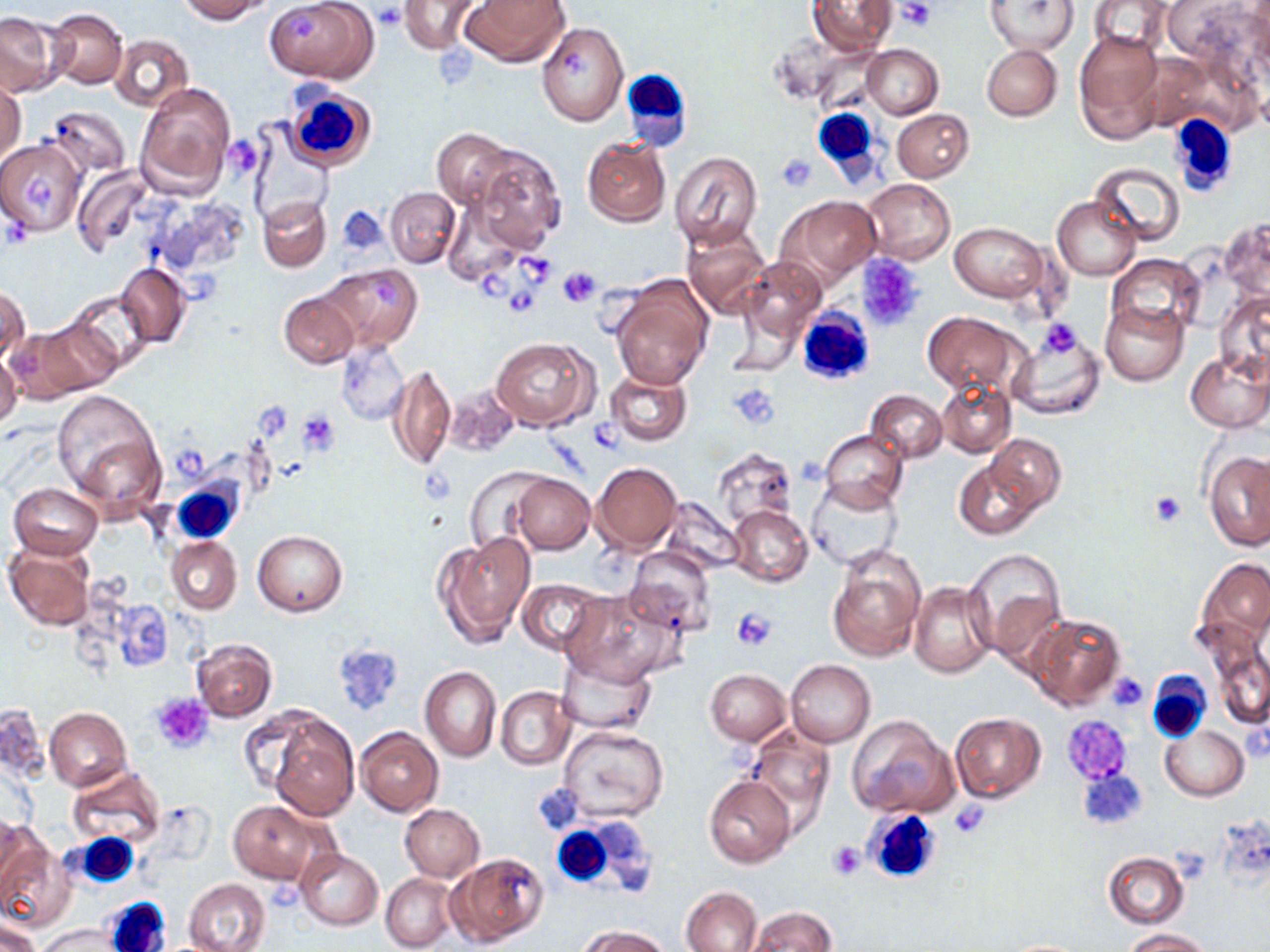
slide-level diagnosis = no evidence of blood parasites
stain = May-Grünwald-Giemsa
uninfected red blood cell locations = approximate bounding boxes as (x1,y1)-(x2,y2) corner pairs in pixels: (179,0)-(272,23), (398,0)-(486,55), (460,0)-(569,67), (808,0)-(896,56), (988,0)-(1078,56), (1089,0)-(1172,54), (1163,0)-(1264,70), (266,1)-(378,84), (47,7)-(128,90), (0,11)-(67,96), (537,22)-(626,125), (1073,31)-(1165,143), (110,34)-(194,112), (862,45)-(942,118), (982,45)-(1061,120), (1135,51)-(1223,134), (1,78)-(25,165), (135,81)-(236,198), (47,104)-(131,178), (893,109)-(974,182), (247,127)-(334,227), (432,127)-(515,207), (581,137)-(670,226), (0,140)-(86,237), (468,144)-(565,253), (670,151)-(764,251), (1089,161)-(1185,246), (72,166)-(151,257), (863,178)-(956,265), (385,186)-(460,267), (152,195)-(250,277), (258,195)-(331,271), (777,195)-(882,286), (1052,196)-(1141,280), (443,200)-(524,284), (1218,217)-(1270,302), (951,221)-(1048,302), (680,223)-(771,320), (1108,253)-(1205,342), (740,256)-(826,344), (319,262)-(422,351), (115,264)-(191,346), (611,282)-(713,390), (1,287)-(30,363), (278,288)-(358,369), (1214,289)-(1270,381), (65,290)-(156,377), (1101,300)-(1190,386), (38,311)-(128,393), (922,311)-(1021,394), (6,323)-(105,403), (1007,330)-(1104,421), (491,336)-(598,431), (336,340)-(409,426), (1184,347)-(1270,431), (0,353)-(22,433), (388,365)-(455,470), (604,368)-(691,447), (937,382)-(1014,457), (445,383)-(522,460), (51,389)-(166,515), (868,389)-(947,462), (819,429)-(907,513), (986,435)-(1065,514), (714,447)-(799,525), (1205,450)-(1270,551), (954,458)-(1044,540), (591,463)-(682,551), (465,468)-(548,554), (511,473)-(594,553), (806,480)-(902,570), (10,483)-(102,558), (661,499)-(744,575), (727,504)-(813,588), (253,530)-(347,616), (433,530)-(536,647), (165,538)-(241,614), (5,541)-(96,630), (827,546)-(926,662), (624,547)-(715,635), (964,547)-(1067,656), (1195,556)-(1270,650), (516,579)-(608,657), (909,581)-(999,680), (562,588)-(681,685), (1026,613)-(1125,710), (190,639)-(278,722), (1212,647)-(1270,729), (558,651)-(657,736), (786,659)-(875,747), (419,666)-(501,761), (706,669)-(792,745), (496,685)-(575,769), (0,703)-(49,782), (45,707)-(132,791), (949,712)-(1045,802), (268,714)-(359,821), (849,715)-(956,818), (558,724)-(668,822), (1161,725)-(1248,800), (356,727)-(443,816), (745,728)-(834,825), (66,766)-(166,847), (704,776)-(796,869), (228,800)-(328,885), (401,805)-(484,882), (0,819)-(39,906), (0,840)-(75,933), (295,848)-(384,930), (448,852)-(549,948), (1103,852)-(1188,929), (381,872)-(458,951), (184,878)-(269,952), (681,886)-(763,951), (746,905)-(838,951), (0,919)-(42,952), (36,923)-(119,952), (581,924)-(669,952), (1123,928)-(1212,951), (994,938)-(1096,951)
image size = 1270×952 pixels
platelet locations = approximate bounding boxes as (x1,y1)-(x2,y2) corner pairs in pixels: (896,2)-(937,29), (373,4)-(407,31), (289,13)-(316,41), (562,48)-(591,80), (224,136)-(264,180), (775,153)-(817,191), (21,173)-(55,210), (339,209)-(386,252), (856,253)-(927,332), (518,256)-(553,286), (559,266)-(599,306), (479,272)-(512,302), (371,277)-(402,306), (509,288)-(539,315), (1037,320)-(1082,359), (732,383)-(779,428), (252,404)-(291,444), (298,412)-(339,455), (588,419)-(626,455), (174,449)-(206,482), (1150,490)-(1185,527), (733,607)-(777,650), (333,642)-(403,716), (1107,673)-(1149,712), (151,693)-(213,753), (1064,716)-(1134,783), (1076,768)-(1148,831), (950,799)-(992,839), (827,841)-(865,880)
field of view = single
modality = light microscopy
magnification = 1000x
preparation = thin blood film
white blood cell locations = approximate bounding boxes as (x1,y1)-(x2,y2) corner pairs in pixels: (615,68)-(686,150), (283,84)-(375,174), (810,108)-(880,180), (1167,115)-(1238,197), (796,306)-(876,386), (169,483)-(242,545), (1145,673)-(1214,741), (861,808)-(943,886), (551,822)-(625,891), (73,833)-(139,886), (103,899)-(170,952)